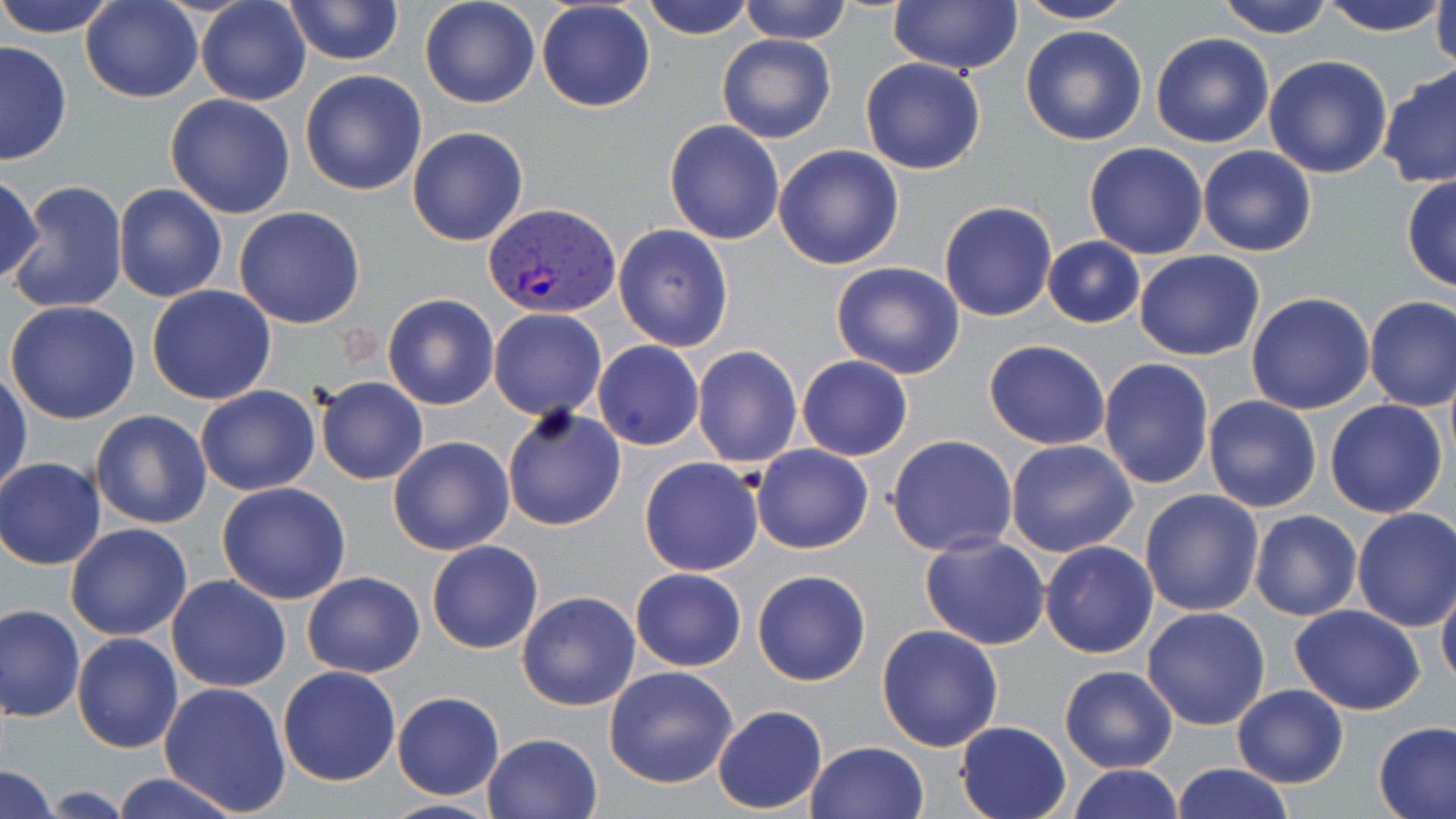
Summary:
  - Coordinate format: approximate bounding boxes as [x1, y1, x2, y2] in pixels
  - Plasmodium vivax-infected red blood cell locations: [485, 201, 622, 319]
  - Uninfected red blood cell locations: [2, 0, 116, 36], [80, 0, 201, 103], [195, 0, 311, 106], [283, 0, 403, 65], [419, 0, 541, 109], [642, 0, 755, 40], [738, 0, 853, 44], [1213, 0, 1336, 40], [1317, 0, 1452, 37], [1429, 0, 1456, 72], [536, 1, 655, 111], [888, 1, 1023, 75], [1014, 1, 1139, 24], [1021, 25, 1148, 147], [1149, 32, 1274, 148], [716, 33, 835, 144], [0, 41, 72, 165], [1263, 55, 1393, 178], [859, 57, 985, 175], [1376, 62, 1456, 189], [299, 69, 427, 195], [164, 93, 296, 219], [663, 119, 785, 245], [407, 126, 528, 247], [1084, 142, 1209, 259], [773, 145, 905, 269], [1197, 146, 1318, 257], [0, 172, 44, 289], [1402, 175, 1456, 293], [7, 181, 129, 316], [113, 184, 227, 302], [939, 202, 1056, 321], [234, 206, 366, 329], [613, 224, 734, 353], [1043, 236, 1144, 327], [1134, 249, 1265, 360], [830, 261, 965, 380], [147, 285, 277, 404], [1246, 292, 1375, 415], [383, 293, 499, 409], [1363, 295, 1456, 412], [5, 300, 143, 424], [488, 309, 607, 421], [984, 340, 1111, 451], [593, 341, 705, 450], [692, 345, 802, 468], [796, 356, 912, 461], [1098, 358, 1214, 488], [1, 370, 31, 495], [316, 378, 428, 484], [196, 385, 319, 496], [1203, 396, 1323, 513], [1325, 400, 1448, 519], [502, 406, 627, 532], [90, 411, 210, 528], [887, 435, 1017, 557], [388, 437, 514, 555], [1006, 438, 1138, 557], [750, 443, 873, 553], [638, 456, 764, 576], [0, 458, 106, 569], [217, 481, 351, 604], [1138, 488, 1264, 618], [1352, 507, 1456, 632], [1249, 510, 1362, 621], [66, 523, 194, 641], [920, 534, 1050, 650], [427, 539, 543, 653], [1041, 540, 1159, 658], [629, 568, 746, 671], [752, 570, 872, 686], [301, 571, 425, 677], [165, 574, 292, 692], [1435, 576, 1456, 695], [516, 590, 641, 711], [1, 603, 84, 722], [1289, 605, 1426, 714], [1142, 606, 1272, 730], [877, 625, 1004, 751], [72, 633, 184, 753], [1060, 665, 1178, 772], [276, 666, 400, 786], [604, 666, 738, 788], [158, 681, 292, 816], [1231, 685, 1349, 787], [391, 690, 504, 800], [713, 705, 827, 814], [955, 720, 1072, 819], [1374, 721, 1456, 819], [482, 732, 603, 819], [807, 741, 929, 819], [1170, 764, 1295, 819], [0, 765, 58, 819], [1069, 765, 1182, 819], [107, 773, 240, 819], [378, 797, 502, 818]
  - Slide-level diagnosis: Plasmodium vivax
  - Stain: May-Grünwald-Giemsa
  - Magnification: 1000x
  - Field of view: one of a larger specimen
  - Image size: 1456×819 pixels
  - Modality: light microscopy
  - Preparation: thin blood smear